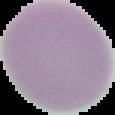
Cell region segmented out of the field of view; the surrounding area is masked to black. Image is 115×115 pixels. From a thin blood smear. Malaria status: uninfected.